Assess this cell for malaria.
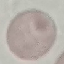

It is uninfected.

Summary:
  - Image type: cell patch, automatically extracted from a larger field of view and resized to 64 × 64 pixels
  - Preparation: thin smear
  - Stain: Giemsa
  - Capture: smartphone camera at the microscope eyepiece